Name the parasite shown.
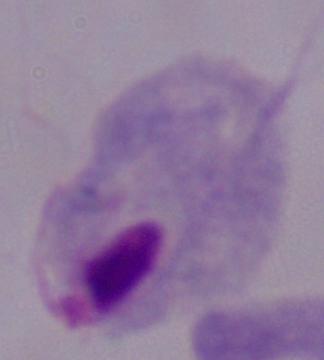
A trichomonad.

1000x magnification. Photomicrograph.